Name the parasite shown.
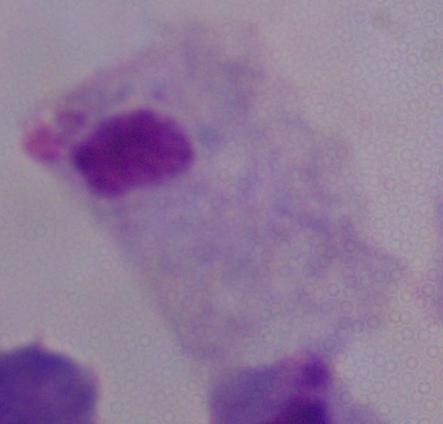

A trichomonad.

Summary:
  - Modality: photomicrograph
  - Magnification: 1000x